Identify the parasite.
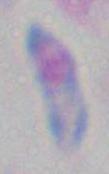
Toxoplasma gondii.

Summary:
  - Magnification: 1000x
  - Modality: micrograph